Assess the morphology of the red blood cells.
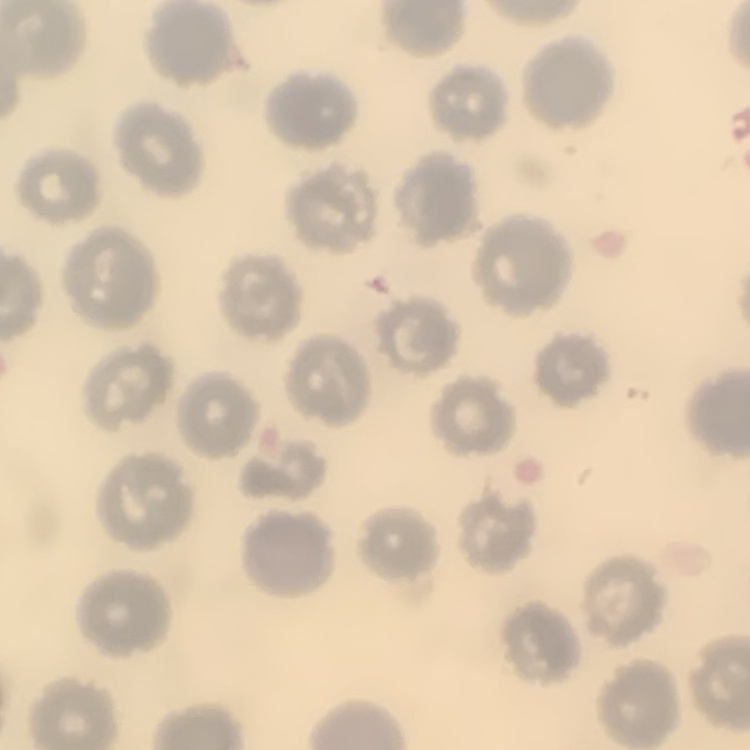
No rouleaux formation.

Summary:
  - Stain: Field's or Giemsa
  - Image type: square crop of a larger photomicrograph
  - Preparation: thin blood film